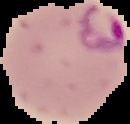

Image is 130×124 pixels. Malaria status: parasitized. From a thin blood smear. Segmented cell region on a black background.